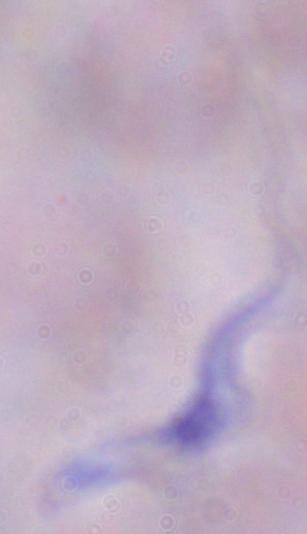
identification: trypanosome
modality: photomicrograph
magnification: 1000x